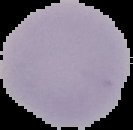
preparation = thin blood film
image type = segmented cell region on a black background
image size = 133×130 pixels
malaria status = uninfected